Give the position of every Plasmodium parasite and every leukocyte.
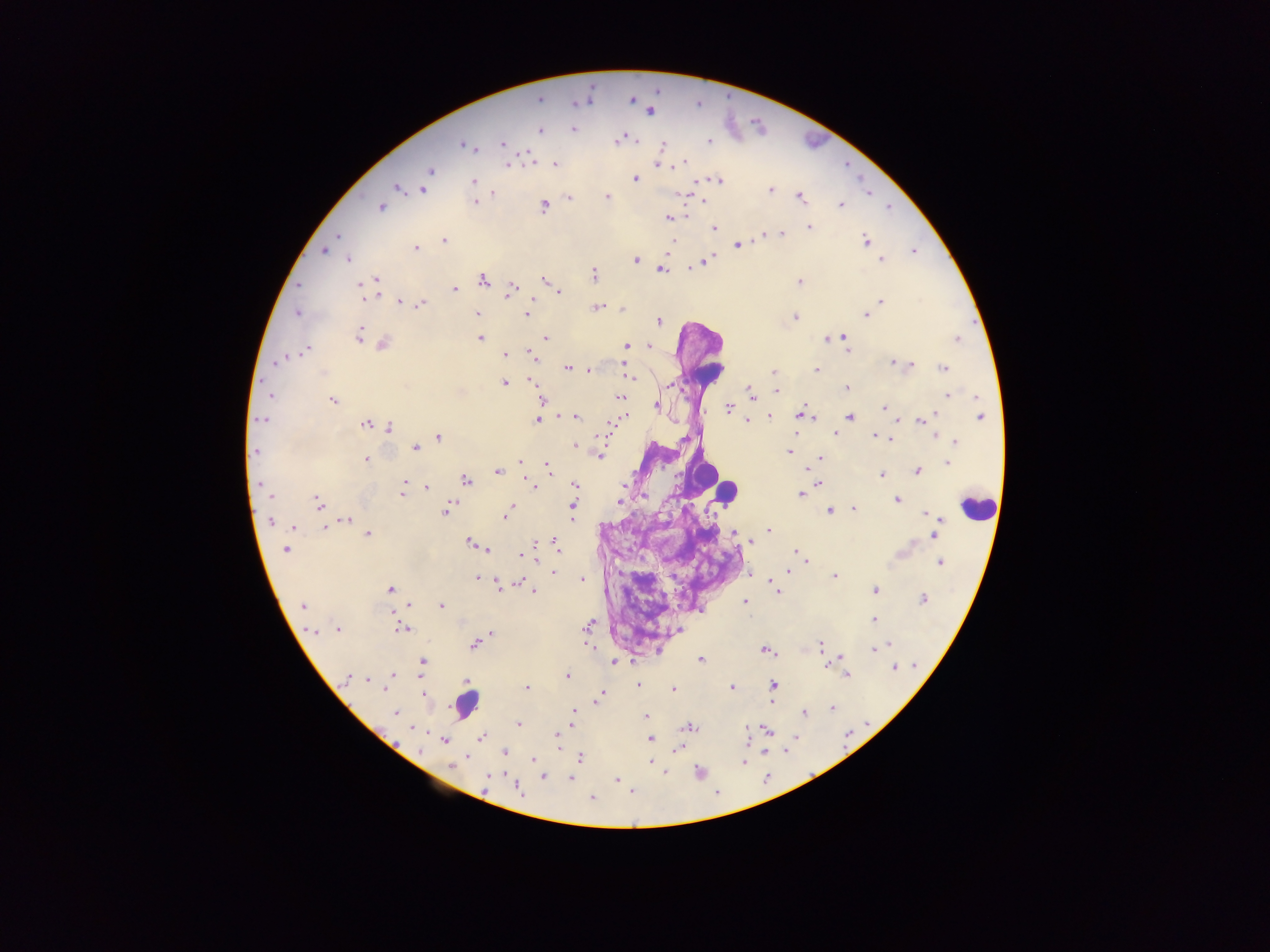

Approximate centers as x y in pixels.
Plasmodium parasites: 539 99; 631 99; 649 110; 573 129; 539 130; 635 139; 619 140; 708 142; 503 144; 466 145; 661 145; 684 162; 554 164; 657 164; 507 165; 430 171; 635 178; 426 180; 473 181; 717 181; 396 187; 423 189; 770 190; 491 192; 682 194; 868 194; 606 196; 799 196; 569 197; 702 201; 474 202; 543 205; 840 205; 381 207; 687 216; 668 217; 808 226; 715 228; 782 232; 765 236; 338 237; 443 241; 865 241; 672 243; 738 245; 414 248; 322 250; 913 250; 348 258; 881 259; 635 260; 705 261; 660 268; 593 274; 375 280; 481 280; 545 280; 798 281; 511 287; 455 289; 560 292; 362 296; 535 300; 399 301; 881 301; 420 304; 598 307; 622 309; 297 313; 476 313; 525 313; 866 314; 795 317; 658 321; 358 335; 365 337; 544 337; 839 337; 844 337; 480 338; 829 338; 957 338; 382 343; 626 345; 648 346; 306 349; 845 349; 504 354; 532 358; 278 360; 892 361; 622 363; 910 365; 568 368; 943 368; 588 370; 773 371; 816 371; 625 374; 630 376; 529 379; 504 383; 670 384; 847 387; 776 391; 270 394; 751 394; 947 394; 619 397; 541 399; 333 400; 656 406; 884 408; 728 409; 800 414; 575 416; 625 416; 808 416; 851 416; 979 416; 768 417; 931 417; 262 419; 537 420; 897 420; 746 421; 921 421; 366 424; 607 424; 388 428; 795 429; 834 432; 875 434; 438 437; 890 438; 955 441; 575 446; 415 447; 255 451; 789 452; 598 455; 366 458; 820 458; 520 462; 947 463; 547 468; 805 470; 916 470; 497 471; 882 474; 466 480; 404 481; 574 484; 819 484; 533 486; 622 487; 403 488; 425 488; 800 494; 402 495; 269 496; 897 499; 619 502; 318 503; 511 505; 573 505; 448 508; 853 509; 830 510; 924 513; 505 516; 572 516; 937 519; 270 520; 346 520; 293 526; 324 528; 769 530; 733 533; 367 534; 932 535; 751 541; 535 542; 471 543; 556 545; 286 549; 487 549; 797 551; 520 555; 800 555; 804 562; 940 562; 789 571; 553 573; 749 574; 834 575; 478 577; 582 580; 518 581; 769 584; 497 585; 390 589; 875 590; 778 591; 535 592; 922 598; 744 602; 302 605; 407 605; 440 605; 874 619; 588 625; 402 628; 312 629; 336 629; 677 630; 489 632; 474 644; 886 644; 820 645; 590 648; 874 649; 766 650; 839 657; 700 659; 614 662; 422 663; 915 664; 894 667; 393 674; 846 675; 566 677; 366 678; 349 679; 465 680; 388 684; 638 685; 773 685; 526 687; 732 687; 673 689; 601 694; 423 695; 597 697; 772 699; 830 707; 396 712; 573 712; 804 712; 646 716; 571 717; 517 723; 688 727; 746 727; 767 730; 557 736; 482 737; 650 739; 444 740; 557 746; 677 747; 503 750; 465 757; 580 758; 533 759; 650 761; 743 762; 450 765; 664 771; 542 776; 488 778; 571 779; 615 779; 485 784; 518 789; 591 798.
Leukocytes: 728 492; 977 508; 465 704.

preparation: thick blood film
country: Ghana
image_size: 1270×952 pixels
field_of_view: single
capture: mobile-phone photograph through a microscope